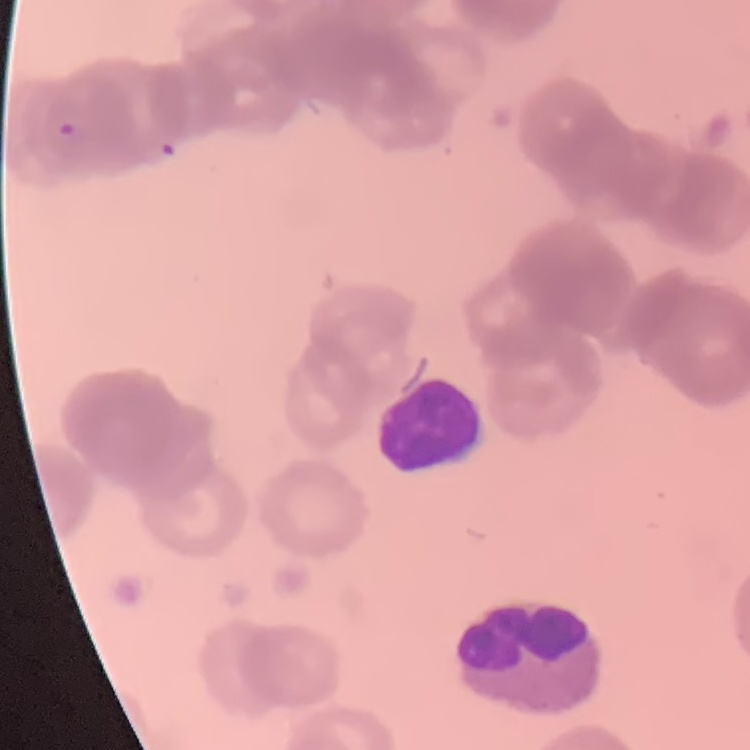

The red blood cells exhibit rouleaux formation. Field's or Giemsa stain. Thin blood film. One tile cut from a larger photomicrograph.